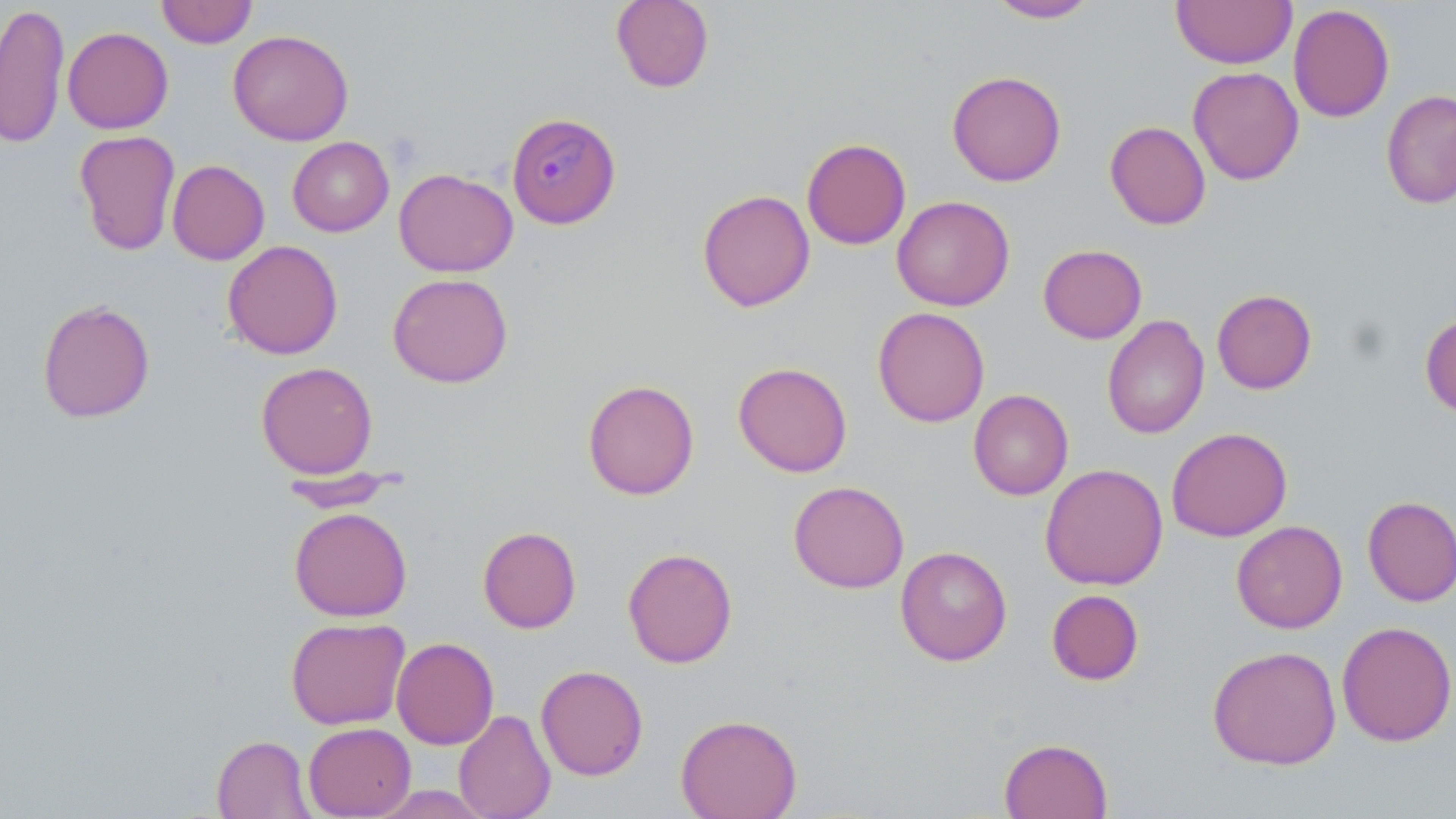
Plasmodium malariae-infected red blood cell locations = approximate bounding boxes as (x1,y1)-(x2,y2) corner pairs in pixels: (506,112)-(620,229)
slide-level diagnosis = Plasmodium malariae
image size = 1456×819 pixels
modality = light microscopy
preparation = thin blood smear
field of view = one of a larger specimen
magnification = 1000x
uninfected red blood cell locations = approximate bounding boxes as (x1,y1)-(x2,y2) corner pairs in pixels: (156,0)-(258,49), (611,0)-(714,93), (987,0)-(1098,23), (1171,0)-(1296,68), (0,3)-(70,149), (1288,4)-(1395,123), (62,26)-(173,134), (227,29)-(354,146), (1188,66)-(1304,186), (947,70)-(1067,187), (1380,89)-(1456,209), (1104,121)-(1211,230), (74,130)-(181,256), (287,136)-(394,237), (801,138)-(911,250), (167,160)-(270,265), (394,168)-(518,277), (697,189)-(815,312), (891,195)-(1015,311), (222,240)-(343,360), (1038,244)-(1147,343), (387,273)-(513,388), (1212,289)-(1317,395), (37,298)-(156,423), (872,306)-(990,427), (1420,312)-(1456,418), (1102,314)-(1210,440), (255,361)-(378,479), (733,361)-(853,478), (582,379)-(700,500), (968,389)-(1073,500), (1166,426)-(1292,542), (1040,463)-(1168,590), (277,470)-(406,512), (788,480)-(909,593), (1362,496)-(1456,607), (289,506)-(413,622), (1231,520)-(1347,634), (478,526)-(582,634), (895,545)-(1012,666), (622,547)-(738,669), (1046,589)-(1144,686), (286,617)-(410,730), (1336,621)-(1456,747), (391,637)-(499,749), (1206,645)-(1342,770), (535,664)-(649,780), (453,708)-(556,819), (675,713)-(802,818), (303,722)-(416,818), (211,735)-(315,818), (999,737)-(1113,819)
stain = May-Grünwald-Giemsa